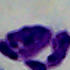
Summary:
  - Modality: micrograph
  - Magnification: 1000x
  - Identification: leukocyte